Classify this cell by malaria status.
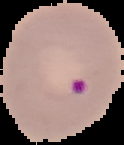
It is parasitized.

From a thin blood film. Cell region segmented out of the field of view; the surrounding area is masked to black. Image is 124×145 pixels.